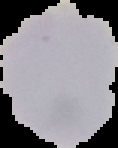
image type = segmented cell region with the area outside set to black
preparation = thin blood smear
result = no Plasmodium parasites detected
image size = 118×148 pixels